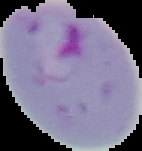

From a thin blood smear. Cell region segmented out of the field of view; the surrounding area is masked to black. Result: Plasmodium parasites detected. Image is 142×151 pixels.